State which cell type is depicted.
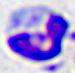
A leukocyte.

Summary:
  - Magnification: 400x
  - Modality: photomicrograph